Locate every malaria parasite and every leukocyte.
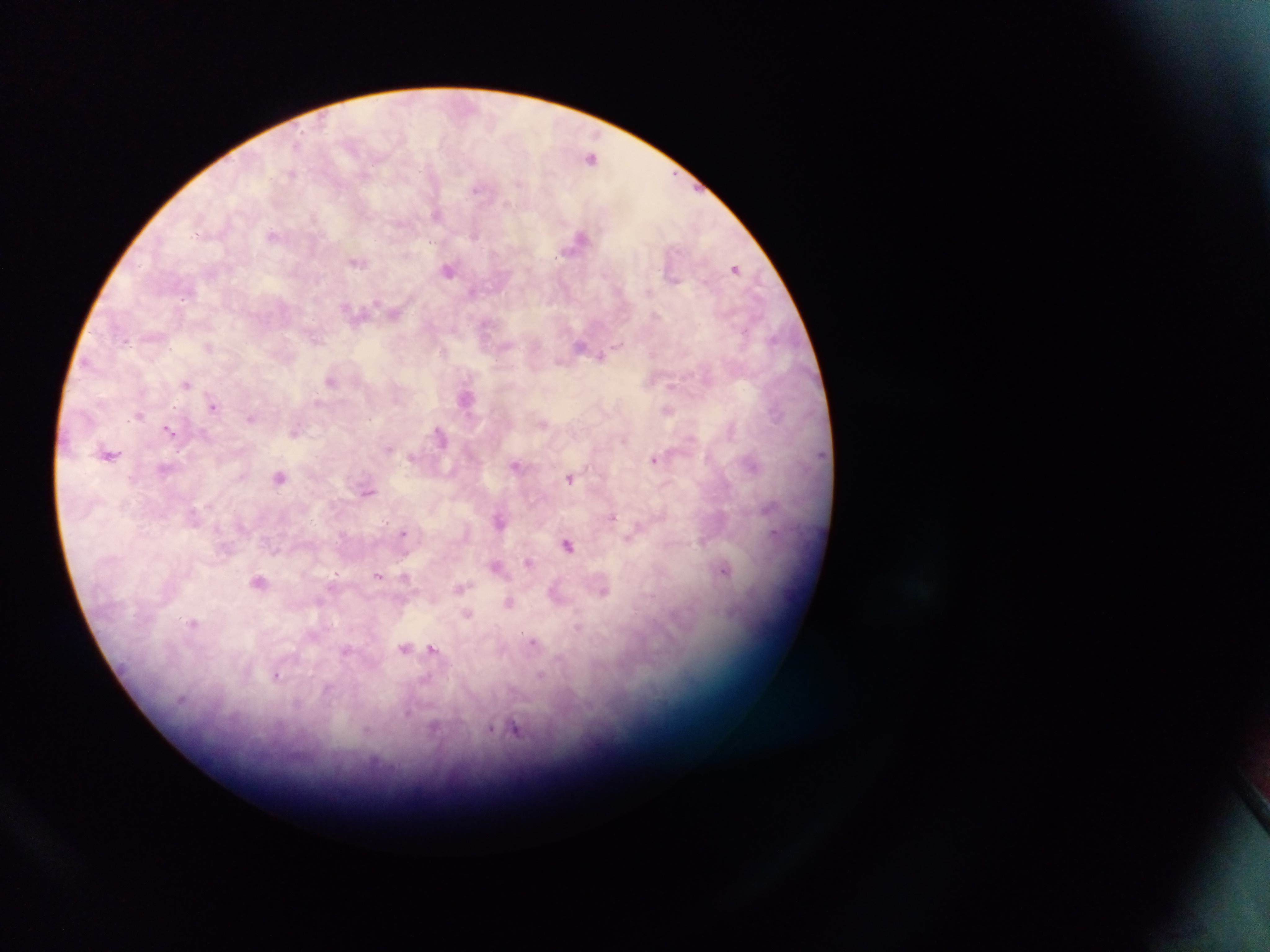

Approximate centers as (x, y) in pixels.
Malaria parasites: (592, 158), (291, 174), (477, 188), (507, 203), (437, 215), (272, 234), (476, 235), (579, 239), (357, 262), (735, 268), (448, 271), (472, 291), (649, 292), (395, 313), (744, 331), (125, 340), (315, 340), (579, 345), (618, 345), (208, 346), (443, 352), (601, 356), (331, 380), (186, 384), (670, 386), (466, 398), (317, 402), (213, 407), (669, 411), (138, 415), (251, 418), (543, 424), (168, 430), (731, 430), (294, 432), (441, 436), (389, 449), (109, 454), (654, 459), (516, 465), (753, 465), (165, 469), (280, 477), (570, 478), (368, 493), (768, 509), (613, 516), (499, 521), (404, 533), (774, 534), (568, 545), (529, 563), (496, 567), (724, 570), (378, 575), (406, 577), (259, 582), (460, 588), (603, 591), (509, 602), (468, 614), (192, 623), (578, 626), (532, 641), (404, 648), (433, 648), (345, 651), (277, 675), (540, 675), (434, 729), (514, 729).
No leukocytes observed.

country = Ghana
field of view = single
image size = 1270×952 pixels
preparation = thick blood film
capture = mobile-phone photograph through a microscope